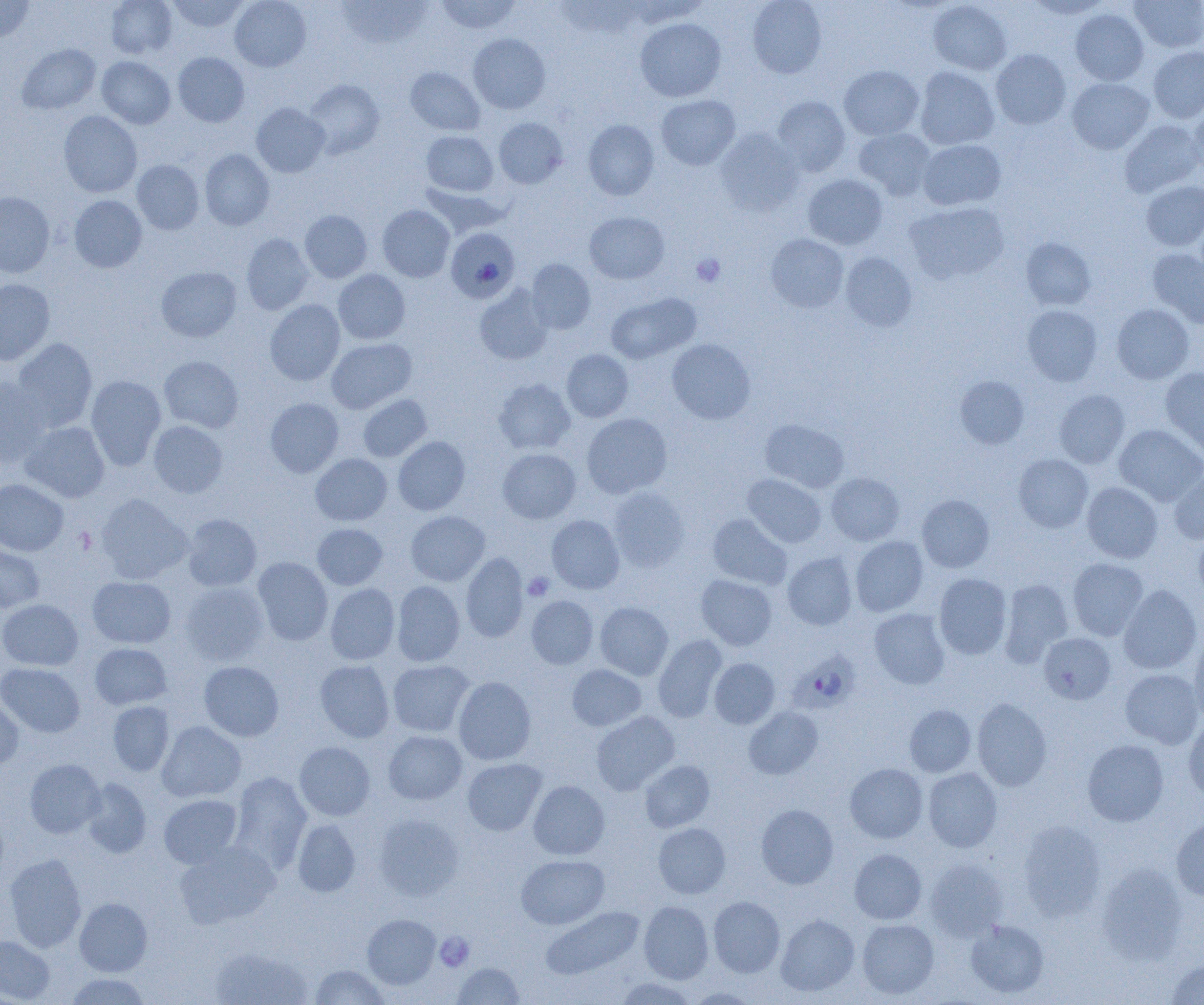

Approximate bounding boxes as named x1/y1/x2/y2 corners in pixels. Platelet locations: (x1=691, y1=253, x2=725, y2=287), (x1=523, y1=572, x2=555, y2=601), (x1=435, y1=933, x2=474, y2=971). Plasmodium falciparum-infected red blood cell locations: (x1=446, y1=227, x2=520, y2=303), (x1=787, y1=648, x2=865, y2=712). Uninfected red blood cell locations: (x1=0, y1=0, x2=34, y2=42), (x1=105, y1=0, x2=178, y2=59), (x1=167, y1=0, x2=251, y2=32), (x1=230, y1=0, x2=311, y2=72), (x1=435, y1=0, x2=522, y2=34), (x1=747, y1=0, x2=827, y2=78), (x1=1024, y1=0, x2=1113, y2=19), (x1=1130, y1=0, x2=1204, y2=52), (x1=336, y1=1, x2=432, y2=49), (x1=555, y1=1, x2=645, y2=40), (x1=928, y1=1, x2=1011, y2=75), (x1=1070, y1=9, x2=1149, y2=85), (x1=635, y1=18, x2=726, y2=102), (x1=468, y1=33, x2=550, y2=114), (x1=17, y1=44, x2=101, y2=115), (x1=1148, y1=46, x2=1204, y2=123), (x1=991, y1=49, x2=1071, y2=130), (x1=173, y1=52, x2=250, y2=127), (x1=96, y1=56, x2=175, y2=129), (x1=839, y1=65, x2=924, y2=140), (x1=915, y1=66, x2=999, y2=150), (x1=405, y1=67, x2=485, y2=136), (x1=1067, y1=78, x2=1154, y2=154), (x1=304, y1=79, x2=385, y2=159), (x1=656, y1=95, x2=740, y2=170), (x1=772, y1=96, x2=851, y2=177), (x1=1189, y1=100, x2=1204, y2=174), (x1=251, y1=102, x2=330, y2=177), (x1=58, y1=111, x2=142, y2=197), (x1=494, y1=118, x2=568, y2=189), (x1=583, y1=119, x2=659, y2=200), (x1=1119, y1=119, x2=1203, y2=198), (x1=714, y1=128, x2=803, y2=216), (x1=854, y1=128, x2=935, y2=200), (x1=421, y1=131, x2=498, y2=196), (x1=918, y1=139, x2=1006, y2=210), (x1=200, y1=149, x2=274, y2=230), (x1=131, y1=160, x2=204, y2=234), (x1=803, y1=174, x2=887, y2=250), (x1=1141, y1=181, x2=1204, y2=251), (x1=421, y1=184, x2=511, y2=238), (x1=0, y1=192, x2=55, y2=277), (x1=69, y1=195, x2=147, y2=272), (x1=905, y1=201, x2=1009, y2=284), (x1=377, y1=205, x2=455, y2=282), (x1=299, y1=210, x2=372, y2=283), (x1=584, y1=211, x2=670, y2=284), (x1=241, y1=233, x2=314, y2=315), (x1=766, y1=234, x2=849, y2=313), (x1=1021, y1=238, x2=1095, y2=310), (x1=1147, y1=248, x2=1204, y2=328), (x1=840, y1=252, x2=917, y2=331), (x1=526, y1=259, x2=596, y2=334), (x1=156, y1=266, x2=241, y2=342), (x1=333, y1=269, x2=410, y2=344), (x1=0, y1=279, x2=55, y2=365), (x1=474, y1=285, x2=553, y2=365), (x1=606, y1=293, x2=700, y2=364), (x1=264, y1=299, x2=345, y2=386), (x1=1112, y1=303, x2=1194, y2=383), (x1=1022, y1=305, x2=1102, y2=386), (x1=12, y1=338, x2=97, y2=432), (x1=326, y1=338, x2=417, y2=413), (x1=666, y1=339, x2=755, y2=424), (x1=562, y1=349, x2=633, y2=422), (x1=159, y1=356, x2=243, y2=433), (x1=1160, y1=367, x2=1204, y2=456), (x1=86, y1=375, x2=166, y2=470), (x1=955, y1=376, x2=1029, y2=449), (x1=0, y1=377, x2=51, y2=469), (x1=494, y1=378, x2=575, y2=454), (x1=1054, y1=390, x2=1129, y2=468), (x1=358, y1=394, x2=432, y2=462), (x1=265, y1=398, x2=344, y2=477), (x1=582, y1=413, x2=672, y2=498), (x1=760, y1=419, x2=849, y2=493), (x1=20, y1=421, x2=109, y2=502), (x1=149, y1=421, x2=228, y2=498), (x1=1114, y1=424, x2=1204, y2=505), (x1=393, y1=436, x2=470, y2=515), (x1=498, y1=448, x2=581, y2=523), (x1=311, y1=454, x2=392, y2=525), (x1=1013, y1=454, x2=1093, y2=533), (x1=1169, y1=468, x2=1204, y2=545), (x1=826, y1=473, x2=905, y2=545), (x1=742, y1=474, x2=826, y2=548), (x1=0, y1=479, x2=69, y2=556), (x1=1082, y1=482, x2=1163, y2=563), (x1=608, y1=487, x2=689, y2=571), (x1=94, y1=494, x2=192, y2=583), (x1=917, y1=494, x2=994, y2=573), (x1=406, y1=511, x2=490, y2=585), (x1=182, y1=513, x2=261, y2=591), (x1=708, y1=514, x2=792, y2=589), (x1=546, y1=515, x2=625, y2=594), (x1=312, y1=523, x2=388, y2=590), (x1=1193, y1=529, x2=1204, y2=605), (x1=850, y1=536, x2=928, y2=616), (x1=0, y1=540, x2=45, y2=613), (x1=461, y1=552, x2=528, y2=642), (x1=782, y1=552, x2=857, y2=630), (x1=252, y1=557, x2=333, y2=645), (x1=1068, y1=558, x2=1148, y2=641), (x1=934, y1=573, x2=1012, y2=659), (x1=696, y1=574, x2=777, y2=650), (x1=87, y1=576, x2=176, y2=648), (x1=998, y1=578, x2=1073, y2=666), (x1=392, y1=581, x2=465, y2=666), (x1=179, y1=582, x2=269, y2=665), (x1=325, y1=583, x2=400, y2=665), (x1=1118, y1=584, x2=1202, y2=674), (x1=527, y1=595, x2=598, y2=669), (x1=0, y1=599, x2=83, y2=671), (x1=595, y1=602, x2=673, y2=680), (x1=869, y1=608, x2=950, y2=689), (x1=1038, y1=633, x2=1116, y2=704), (x1=1189, y1=634, x2=1204, y2=725), (x1=653, y1=635, x2=727, y2=722), (x1=90, y1=643, x2=172, y2=709), (x1=709, y1=657, x2=780, y2=728), (x1=315, y1=659, x2=395, y2=742), (x1=388, y1=660, x2=474, y2=736), (x1=199, y1=661, x2=284, y2=741), (x1=0, y1=663, x2=85, y2=737), (x1=566, y1=664, x2=647, y2=731), (x1=1120, y1=668, x2=1203, y2=748), (x1=453, y1=676, x2=536, y2=765), (x1=0, y1=693, x2=23, y2=770), (x1=972, y1=698, x2=1052, y2=791), (x1=108, y1=701, x2=174, y2=776), (x1=904, y1=705, x2=976, y2=777), (x1=743, y1=706, x2=823, y2=779), (x1=591, y1=711, x2=679, y2=795), (x1=1183, y1=719, x2=1204, y2=801), (x1=157, y1=721, x2=246, y2=802), (x1=383, y1=731, x2=467, y2=804), (x1=1082, y1=739, x2=1168, y2=826), (x1=294, y1=741, x2=375, y2=820), (x1=25, y1=758, x2=105, y2=838), (x1=462, y1=758, x2=546, y2=835), (x1=640, y1=760, x2=714, y2=832), (x1=845, y1=763, x2=928, y2=843), (x1=923, y1=767, x2=1002, y2=852), (x1=229, y1=771, x2=312, y2=872), (x1=81, y1=778, x2=151, y2=858), (x1=528, y1=780, x2=610, y2=859), (x1=159, y1=794, x2=242, y2=868), (x1=756, y1=804, x2=838, y2=889), (x1=373, y1=813, x2=464, y2=901), (x1=1171, y1=817, x2=1204, y2=900), (x1=293, y1=819, x2=360, y2=897), (x1=1018, y1=821, x2=1107, y2=920), (x1=653, y1=823, x2=731, y2=898), (x1=174, y1=841, x2=280, y2=929), (x1=849, y1=848, x2=926, y2=924), (x1=4, y1=853, x2=86, y2=953), (x1=516, y1=855, x2=609, y2=929), (x1=924, y1=858, x2=1008, y2=940), (x1=1097, y1=863, x2=1188, y2=965), (x1=708, y1=896, x2=785, y2=977), (x1=75, y1=897, x2=152, y2=976), (x1=639, y1=900, x2=713, y2=983), (x1=541, y1=906, x2=644, y2=980), (x1=362, y1=914, x2=440, y2=989), (x1=776, y1=915, x2=859, y2=996), (x1=857, y1=919, x2=939, y2=999), (x1=965, y1=919, x2=1049, y2=998), (x1=0, y1=935, x2=55, y2=1004), (x1=208, y1=946, x2=314, y2=1005), (x1=1165, y1=958, x2=1204, y2=1004), (x1=454, y1=963, x2=524, y2=1004), (x1=310, y1=964, x2=389, y2=1004), (x1=63, y1=973, x2=152, y2=1004), (x1=615, y1=976, x2=697, y2=1005), (x1=685, y1=987, x2=761, y2=1004). Slide-level diagnosis: Plasmodium falciparum. Optical microscopy. Thin blood smear. Image is 1204×1005 pixels. Captured at 1000x magnification. One field of a larger specimen.